Report the malaria status of this cell.
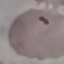

It is parasitized.

stain = Giemsa
preparation = thin blood film
capture = smartphone through the microscope eyepiece
image type = cell patch, automatically extracted from a larger field of view and resized to 64 × 64 pixels